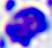
{
  "modality": "micrograph",
  "magnification": "400x",
  "identification": "leukocyte"
}